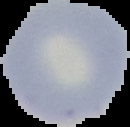
Summary:
  - Image type: segmented cell region with the area outside set to black
  - Image size: 130×127 pixels
  - Preparation: thin blood film
  - Malaria status: uninfected